Give the position of every leukocyte.
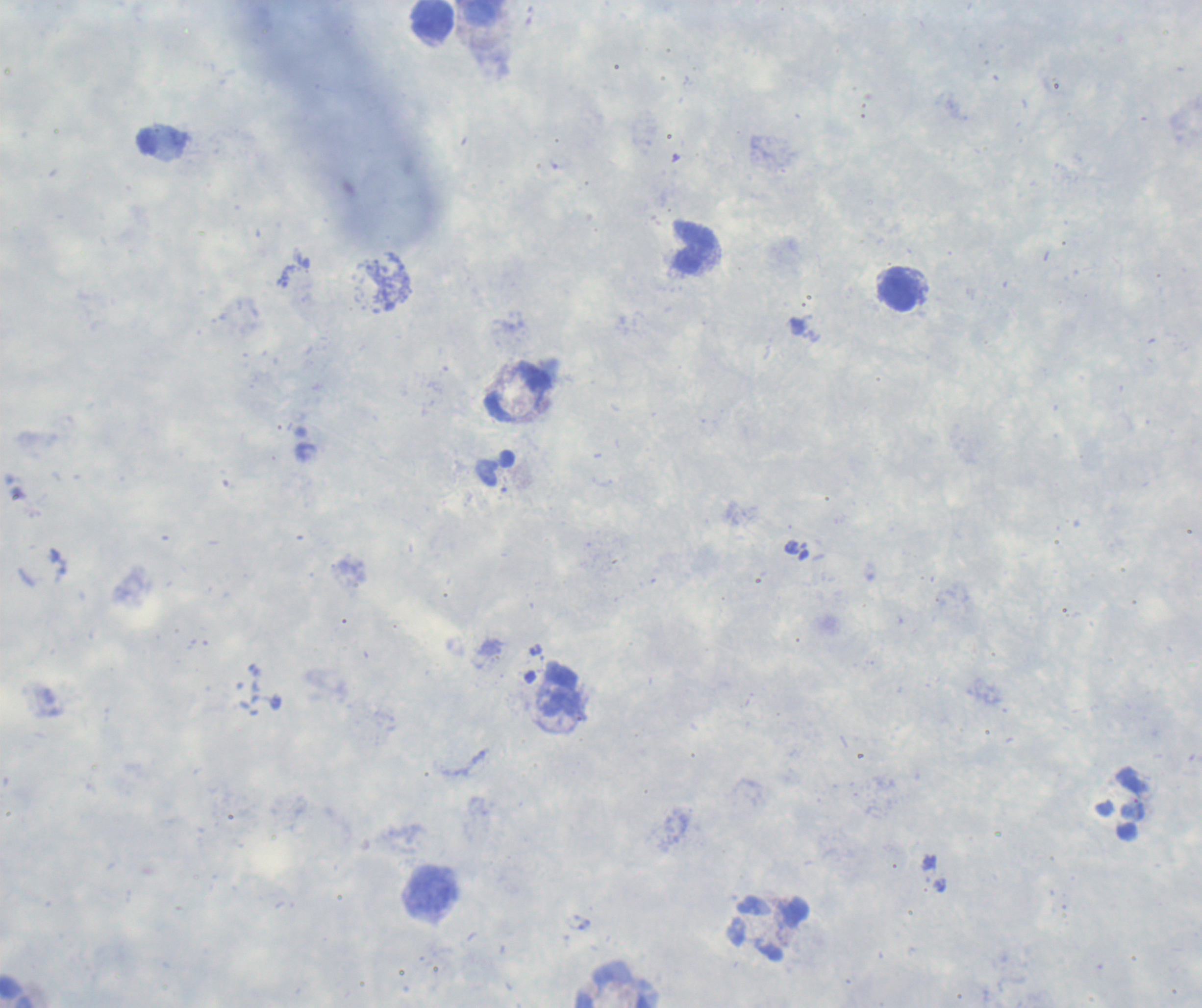
Approximate centers as (x, y) in pixels.
Leukocytes: (483, 13), (433, 20), (693, 246), (900, 289), (562, 702), (430, 891), (768, 928), (617, 984), (17, 991).

Image is 1202×1008 pixels. One field from this slide. Coloration quality: good. Thick smear of blood. Background quality: unsatisfactory. Captured at 100x magnification. Previously used in a real diagnosis. Result: no malaria parasites detected. Romanowsky-stained preparation.